Assess this cell for malaria.
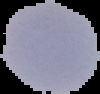
Parasitized.

Summary:
  - Image size: 100×94 pixels
  - Preparation: thin blood film
  - Image type: cell region segmented out of the field of view; surrounding area masked to black